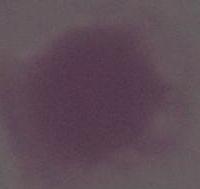 1000x magnification. Micrograph. A red blood cell is seen.